Point out every malaria parasite.
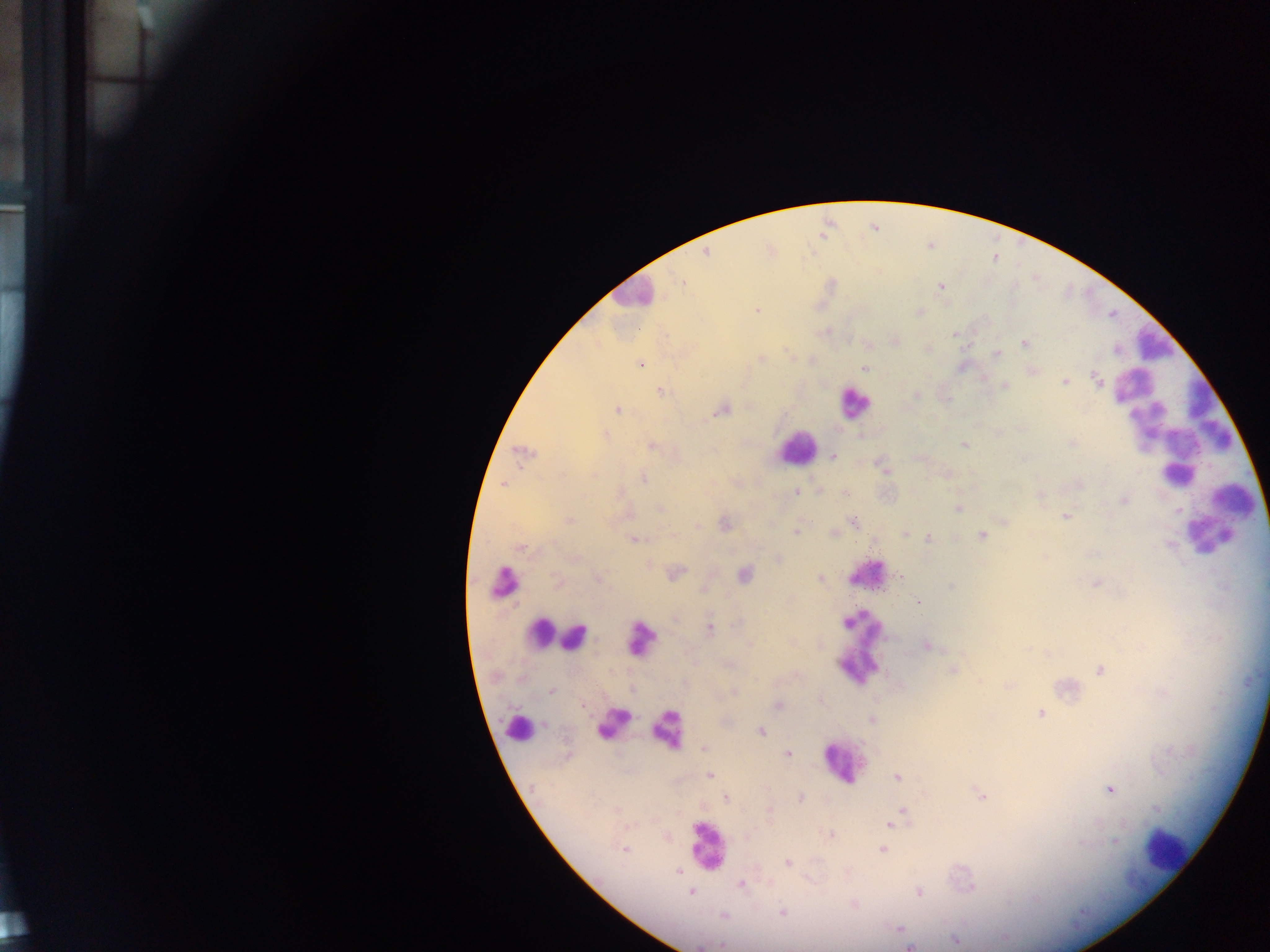

Approximate centers as [x, y] in pixels.
Malaria parasites: [706, 253], [941, 287], [757, 309], [919, 312], [955, 334], [1025, 343], [998, 354], [761, 358], [640, 364], [865, 368], [1097, 379], [1065, 382], [1005, 385], [660, 391], [916, 394], [617, 410], [722, 410], [606, 435], [1072, 444], [965, 445], [653, 446], [523, 452], [834, 457], [886, 471], [643, 479], [503, 484], [1079, 484], [796, 492], [845, 492], [1041, 495], [1123, 500], [958, 508], [660, 509], [1066, 517], [570, 520], [854, 521], [726, 525], [698, 526], [796, 532], [906, 534], [981, 535], [928, 538], [634, 539], [1169, 543], [519, 548], [778, 558], [675, 572], [745, 575], [901, 576], [820, 578], [598, 579], [1097, 583], [558, 584], [703, 589], [919, 602], [739, 623], [710, 628], [750, 644], [927, 645], [953, 670], [1099, 670], [551, 690], [734, 691], [778, 706], [1040, 714], [872, 719], [761, 732], [705, 748], [788, 754], [710, 776], [897, 777], [1109, 789], [981, 796], [726, 798], [801, 798], [769, 810], [902, 810], [890, 825], [830, 835], [1115, 841], [624, 849], [883, 850], [788, 863], [678, 872], [740, 884], [971, 887], [691, 892], [919, 892], [782, 912], [724, 916], [898, 928], [955, 940], [722, 945], [909, 947].

field of view = single
country = Ghana
capture = mobile-phone photograph through a microscope
leukocyte locations = approximate centers as [x, y] in pixels: [631, 294], [1152, 345], [853, 403], [1177, 434], [796, 448], [1239, 508], [1210, 533], [865, 575], [501, 582], [536, 633], [637, 637], [575, 638], [857, 642], [612, 721], [669, 728], [517, 730], [840, 765], [706, 846], [1164, 849]
image size = 1270×952 pixels
preparation = thick blood smear